Classify this cell by malaria status.
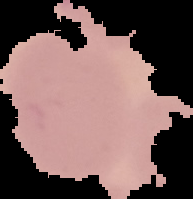

Uninfected.

From a thin blood film. Segmented cell region on a black background. Image is 193×199 pixels.